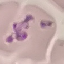
Malaria status: uninfected. Thin blood smear. Automatically extracted cell patch, resized to 64 × 64 pixels. Acquired by smartphone through the microscope eyepiece. Giemsa stain.